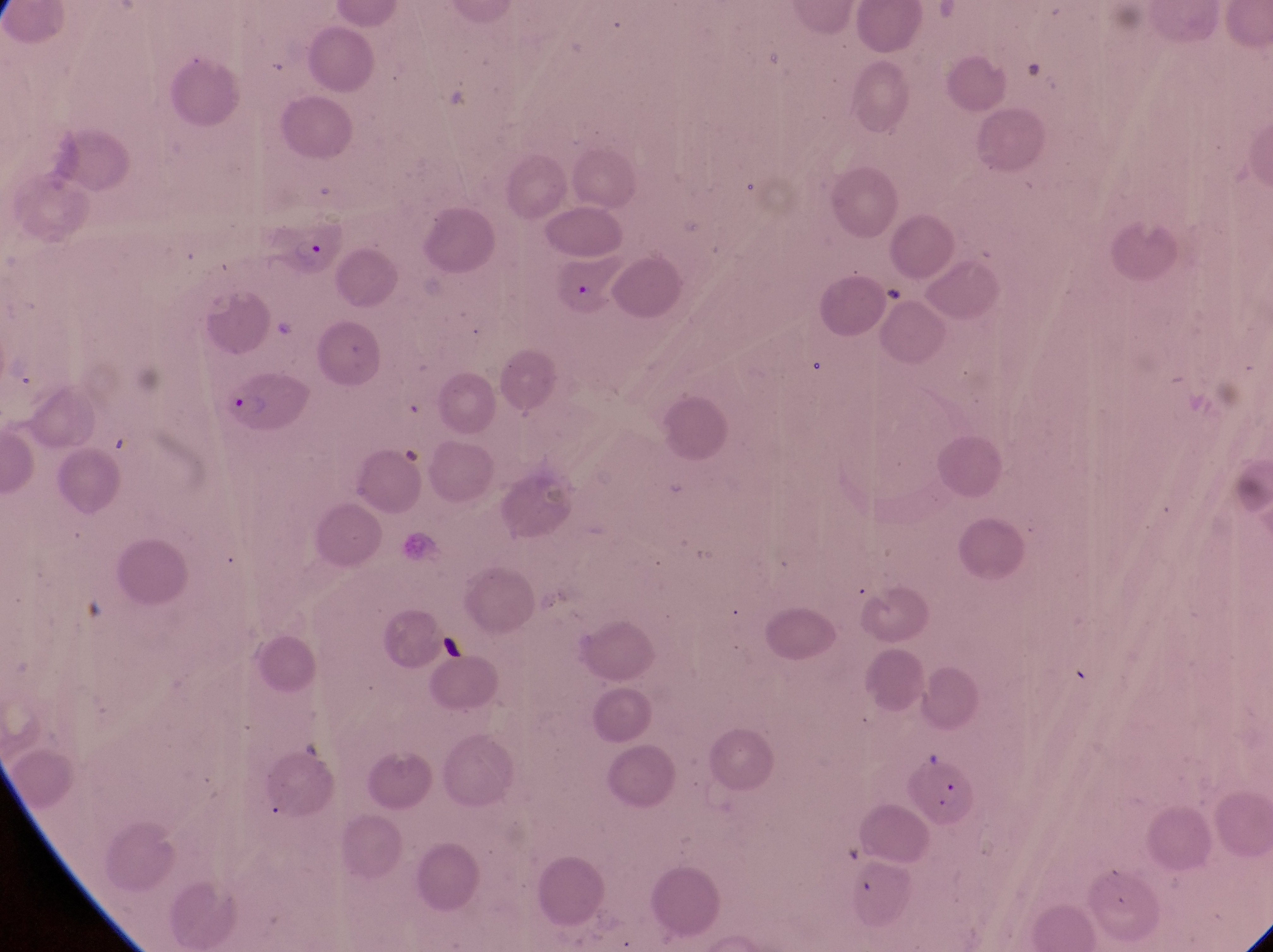
Approximate bounding boxes as [left, top, right, bottom] in pixels. Parasitised red blood cell locations: [272, 215, 350, 278], [224, 374, 312, 441]. Image is 1273×952 pixels. Thin blood smear. Captured by a smartphone held over the eyepiece of an Olympus CX-23 microscope. Sample from Uganda. Magnification of 1000x. One field of view.